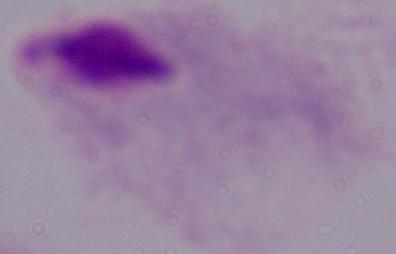

{
  "identification": "trichomonad",
  "modality": "micrograph",
  "magnification": "1000x"
}